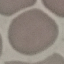
malaria status = uninfected
capture = smartphone through the microscope eyepiece
preparation = thin blood film
image type = automatically extracted cell patch, resized to 64 × 64 pixels
stain = Giemsa